Outline each Plasmodium ovale-infected red blood cell.
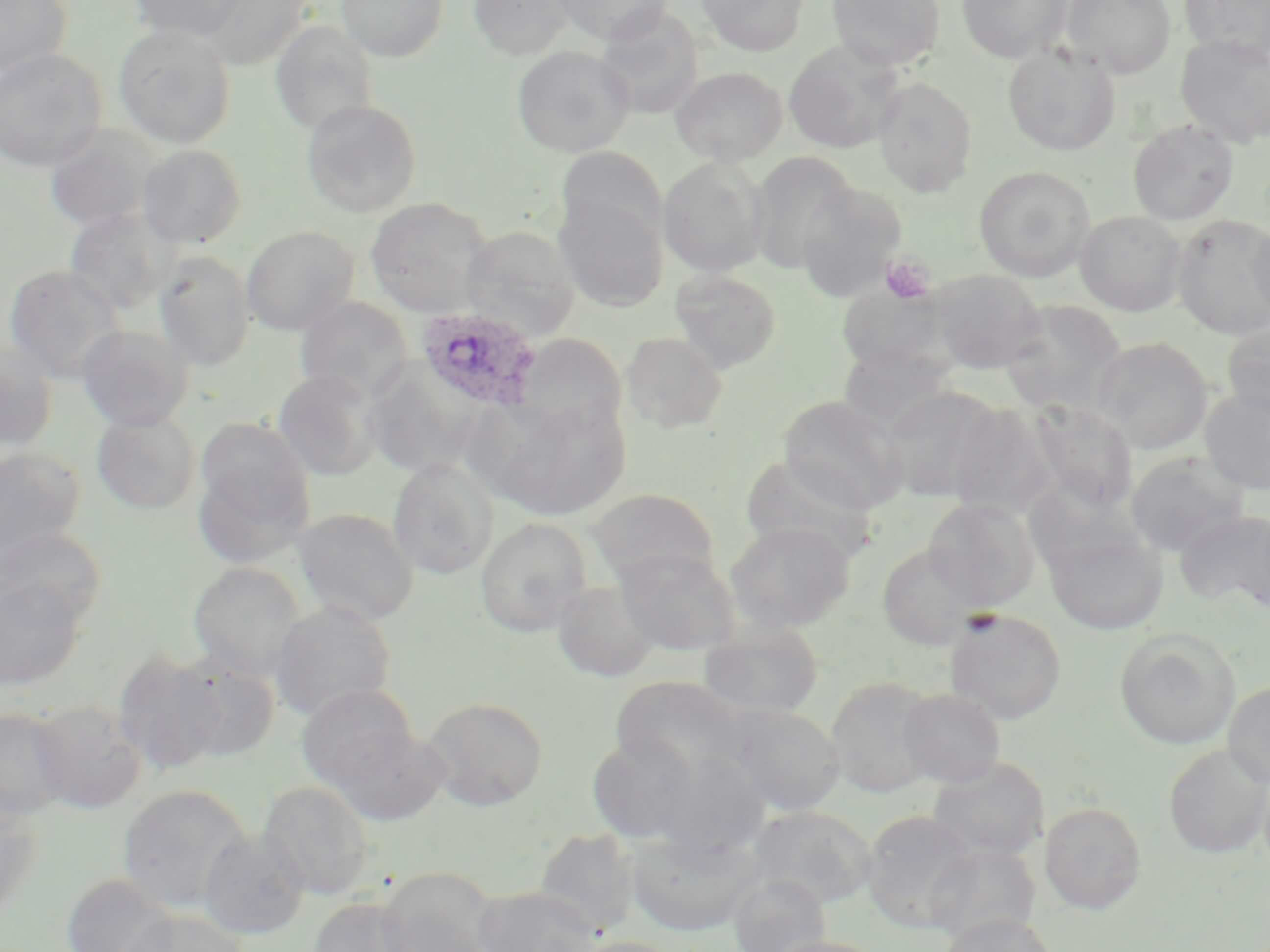

Approximate bounding boxes as (x1, y1, x2, y2) in pixels.
Plasmodium ovale-infected red blood cells: (415, 305, 544, 412).

Platelet locations: (881, 255, 935, 304). Uninfected red blood cell locations: (0, 0, 72, 78), (128, 0, 248, 43), (200, 0, 312, 69), (336, 0, 449, 62), (468, 0, 575, 60), (552, 0, 673, 45), (696, 0, 808, 57), (827, 0, 945, 71), (957, 0, 1072, 64), (1060, 0, 1177, 79), (1179, 0, 1270, 61), (593, 5, 705, 121), (270, 20, 379, 135), (113, 24, 236, 149), (1175, 35, 1270, 149), (783, 40, 904, 154), (512, 45, 634, 157), (1002, 45, 1121, 156), (0, 48, 106, 172), (670, 66, 788, 165), (873, 78, 977, 197), (301, 98, 423, 217), (1128, 120, 1240, 225), (43, 125, 159, 234), (136, 144, 248, 247), (556, 146, 668, 251), (746, 152, 858, 272), (657, 156, 770, 278), (974, 165, 1095, 282), (795, 182, 907, 300), (553, 194, 669, 312), (364, 197, 494, 318), (63, 208, 174, 316), (1075, 210, 1188, 316), (1170, 214, 1270, 340), (1247, 218, 1270, 328), (241, 226, 359, 336), (459, 226, 581, 341), (153, 250, 255, 371), (3, 264, 126, 383), (928, 268, 1047, 374), (669, 270, 781, 374), (837, 284, 955, 377), (294, 295, 414, 404), (999, 299, 1128, 416), (1221, 320, 1270, 417), (75, 324, 193, 431), (621, 332, 728, 434), (510, 334, 627, 441), (1092, 336, 1214, 453), (0, 342, 59, 453), (837, 342, 958, 433), (362, 362, 485, 478), (273, 369, 383, 480), (880, 385, 1006, 502), (1200, 386, 1270, 494), (481, 395, 631, 521), (778, 395, 910, 515), (1030, 401, 1138, 511), (947, 403, 1061, 521), (91, 410, 200, 514), (195, 417, 317, 549), (0, 446, 86, 561), (1125, 450, 1248, 556), (739, 454, 879, 564), (387, 458, 500, 579), (1022, 478, 1144, 571), (588, 487, 719, 587), (922, 498, 1040, 611), (292, 507, 419, 627), (1175, 508, 1270, 611), (475, 517, 592, 637), (724, 521, 856, 633), (0, 526, 106, 630), (1042, 529, 1169, 635), (876, 543, 984, 650), (613, 548, 741, 655), (188, 561, 308, 681), (0, 574, 88, 691), (551, 580, 661, 682), (268, 600, 397, 722), (944, 609, 1068, 724), (698, 621, 824, 719), (1114, 628, 1241, 750), (111, 649, 229, 775), (175, 656, 280, 762), (609, 674, 755, 792), (824, 675, 941, 798), (1222, 680, 1270, 788), (296, 683, 420, 795), (898, 688, 1006, 788), (421, 695, 549, 811), (30, 700, 147, 814), (718, 701, 846, 816), (0, 706, 72, 821), (320, 721, 451, 827), (585, 732, 705, 844), (1164, 745, 1270, 859), (927, 756, 1050, 861), (257, 781, 374, 900), (116, 783, 256, 912), (0, 793, 43, 918), (1039, 802, 1146, 914), (746, 805, 878, 908), (861, 810, 980, 932), (534, 827, 643, 934), (623, 827, 765, 936), (197, 830, 310, 940), (923, 842, 1041, 943), (373, 868, 499, 952), (61, 873, 182, 952), (728, 873, 831, 951), (473, 885, 603, 952), (308, 897, 424, 952), (124, 909, 251, 952), (939, 912, 1057, 952), (762, 935, 888, 952), (567, 936, 688, 952). Slide-level diagnosis: Plasmodium ovale. Captured at 1000x magnification. Thin blood smear. May-Grünwald-Giemsa-stained preparation. Light microscopy. Single field of view. Image is 1270×952 pixels.